Assess the morphology of the erythrocytes.
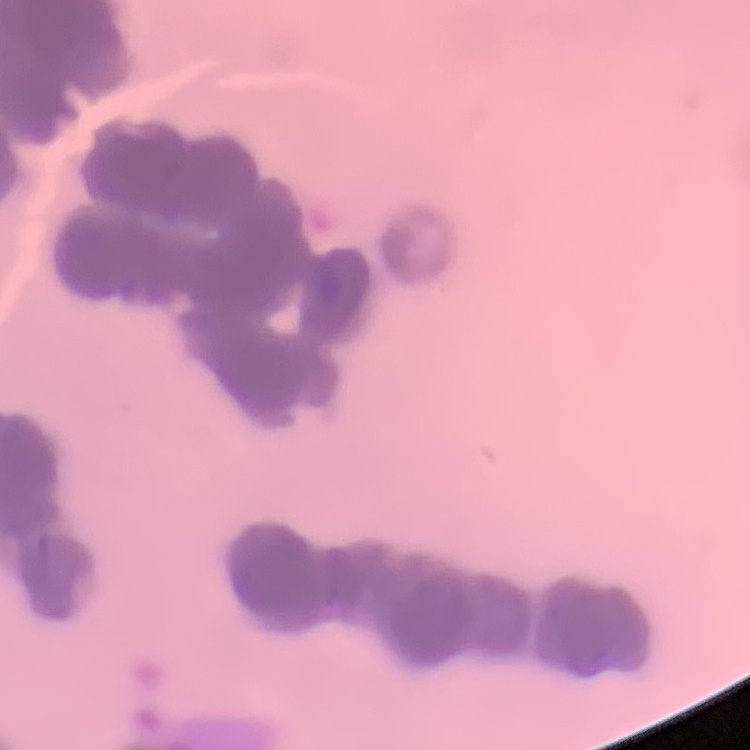

They show rouleaux formation.

Square crop of a larger photomicrograph. Field's or Giemsa stain. Thin peripheral smear.